Outline every leukocyte.
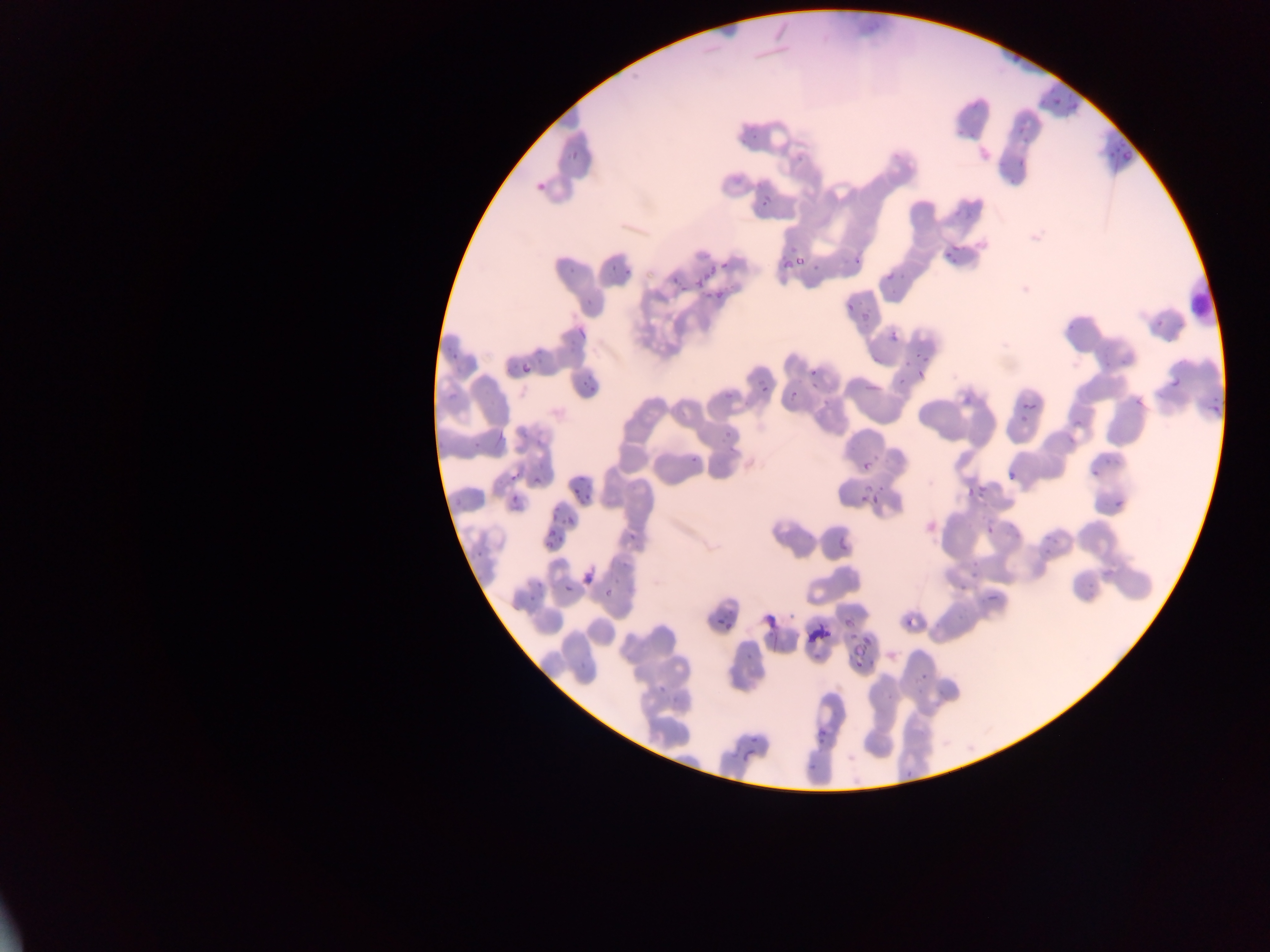
Approximate bounding boxes as {left, top, right, bottom} in pixels.
Leukocytes: {1181, 267, 1211, 329}.

image size = 1270×952 pixels
malaria parasite locations = approximate bounding boxes as {left, top, right, bottom} in pixels: {1040, 82, 1054, 103}, {1064, 94, 1079, 114}, {739, 122, 762, 145}, {1014, 122, 1031, 141}, {1105, 139, 1129, 160}, {567, 147, 585, 161}, {1013, 160, 1033, 173}, {1002, 175, 1013, 186}, {534, 179, 552, 197}, {753, 197, 768, 211}, {943, 242, 961, 262}, {775, 248, 813, 276}, {603, 253, 620, 277}, {848, 254, 861, 266}, {567, 255, 582, 277}, {686, 255, 710, 279}, {718, 258, 732, 273}, {617, 264, 630, 284}, {881, 266, 902, 290}, {666, 269, 681, 290}, {700, 283, 725, 308}, {583, 298, 598, 309}, {843, 302, 855, 311}, {856, 309, 876, 325}, {1152, 318, 1161, 330}, {1063, 319, 1071, 327}, {574, 323, 587, 340}, {888, 328, 903, 345}, {916, 349, 936, 362}, {446, 350, 463, 364}, {1116, 353, 1127, 370}, {903, 360, 911, 366}, {1102, 360, 1111, 371}, {1169, 364, 1188, 389}, {518, 365, 529, 378}, {745, 365, 776, 395}, {807, 367, 820, 382}, {579, 368, 597, 391}, {722, 371, 747, 408}, {917, 372, 931, 384}, {894, 377, 905, 388}, {788, 384, 798, 401}, {1131, 398, 1140, 408}, {1019, 399, 1043, 426}, {1207, 399, 1223, 418}, {725, 423, 747, 446}, {493, 424, 514, 449}, {468, 433, 483, 454}, {691, 442, 713, 473}, {855, 456, 876, 475}, {1101, 457, 1115, 468}, {1006, 463, 1022, 482}, {1087, 463, 1099, 475}, {507, 469, 522, 484}, {531, 472, 544, 486}, {856, 480, 892, 507}, {963, 480, 993, 501}, {569, 482, 594, 500}, {1108, 485, 1136, 510}, {507, 491, 526, 509}, {549, 502, 559, 519}, {563, 513, 578, 529}, {980, 519, 994, 535}, {836, 521, 860, 554}, {621, 527, 645, 554}, {1039, 529, 1061, 552}, {542, 530, 559, 549}, {472, 552, 485, 563}, {962, 560, 982, 576}, {1100, 564, 1113, 582}, {578, 569, 602, 588}, {1076, 577, 1096, 606}, {956, 580, 971, 590}, {557, 582, 570, 599}, {600, 583, 617, 600}, {519, 586, 537, 605}, {983, 586, 1008, 604}, {841, 615, 863, 635}, {762, 616, 776, 632}, {715, 618, 732, 644}, {901, 618, 914, 631}, {853, 631, 879, 648}, {743, 651, 754, 669}, {850, 653, 867, 670}, {913, 661, 942, 693}, {654, 681, 668, 693}, {813, 724, 832, 744}, {739, 748, 760, 763}, {804, 754, 822, 776}, {899, 759, 921, 790}
capture = mobile-phone photograph through a microscope
field of view = single
preparation = thin blood film
country = Ghana